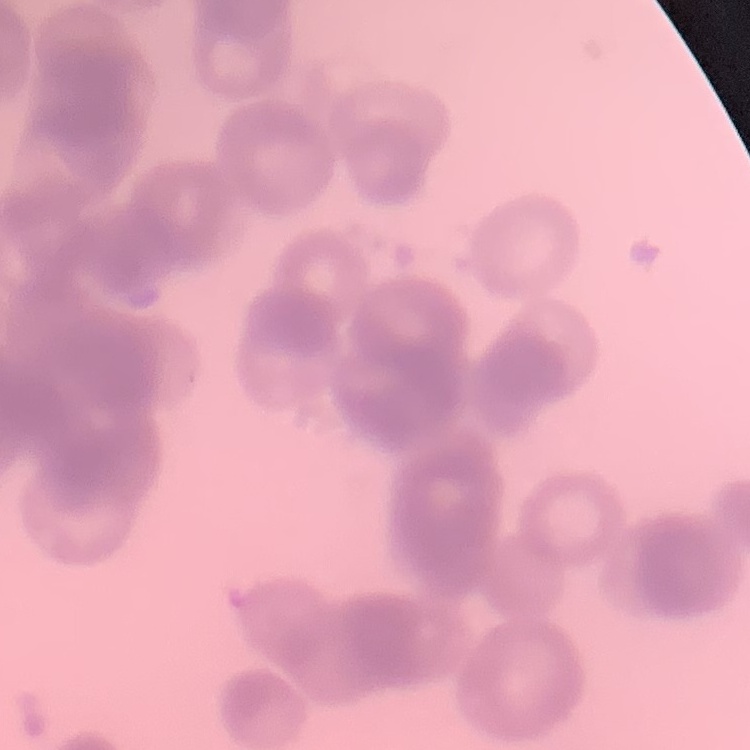 The red blood cells exhibit rouleaux formation. Stained with either Field's or Giemsa. One tile cut from a larger photomicrograph. Thin peripheral smear.